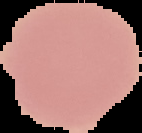

Result: no Plasmodium parasites seen. Image is 142×133 pixels. Segmented cell region on a black background. From a thin blood film.